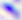
Toxoplasma gondii is shown. Micrograph. Captured at 400x magnification.